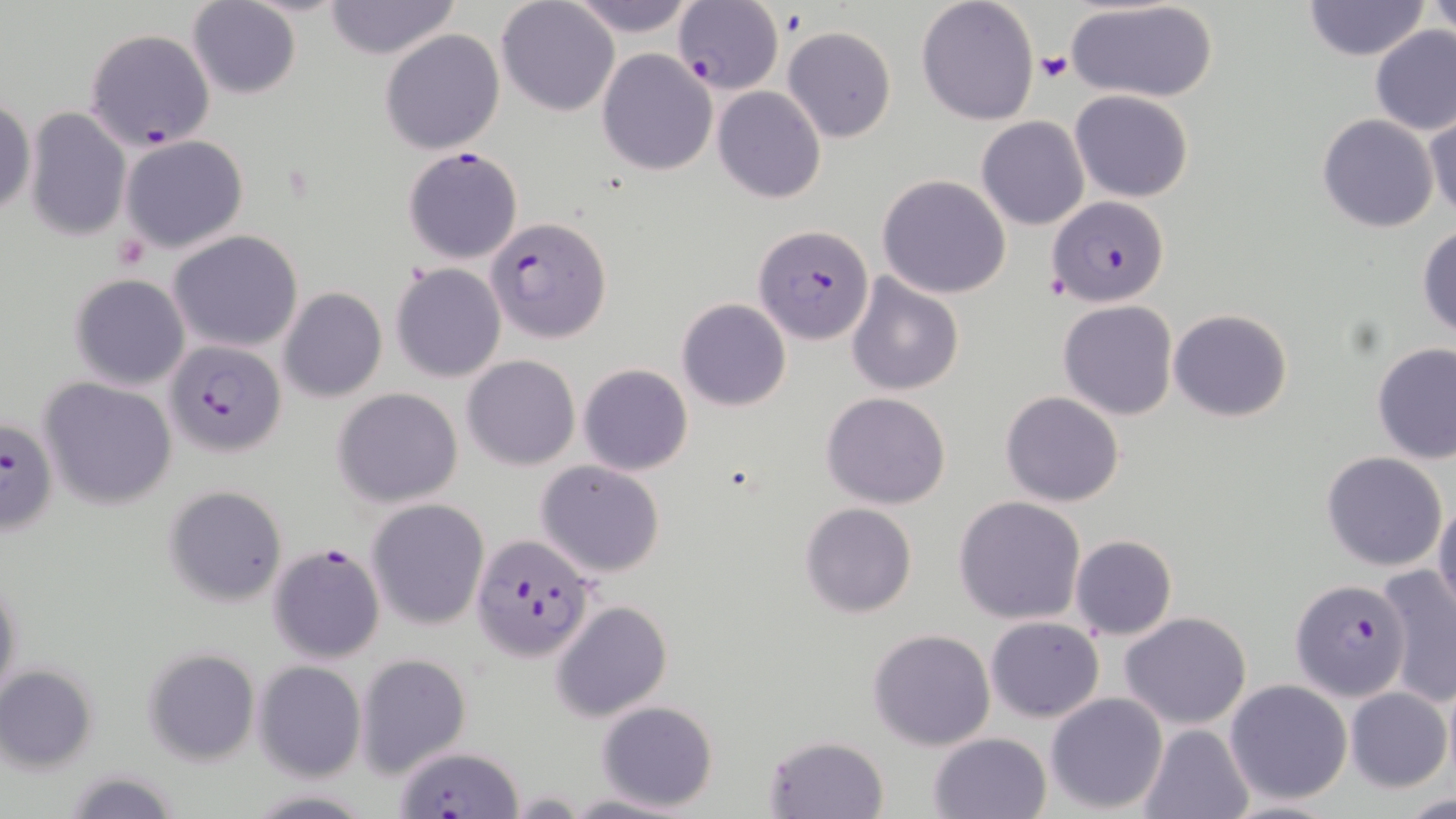 Approximate bounding boxes as (x1,y1)-(x2,y2) corner pairs in pixels. Plasmodium falciparum-infected red blood cell locations: (673,1)-(783,95), (85,28)-(214,150), (402,147)-(524,264), (1050,196)-(1169,305), (487,214)-(612,344), (754,224)-(874,347), (167,338)-(287,455), (0,415)-(59,533), (470,533)-(597,661), (267,543)-(385,666), (1290,579)-(1409,702), (395,747)-(520,818). Uninfected red blood cell locations: (496,0)-(619,116), (566,0)-(699,37), (916,0)-(1039,124), (1303,0)-(1430,61), (1425,0)-(1455,38), (187,1)-(302,100), (322,1)-(462,60), (1068,1)-(1219,104), (783,25)-(897,142), (1369,25)-(1456,136), (380,29)-(505,154), (596,47)-(718,176), (713,86)-(825,204), (1070,90)-(1195,203), (0,96)-(35,219), (25,107)-(130,242), (1423,109)-(1456,221), (1317,114)-(1439,234), (976,116)-(1089,230), (120,135)-(248,253), (877,175)-(1012,299), (1416,224)-(1456,340), (170,231)-(302,352), (391,263)-(505,382), (845,272)-(965,395), (69,274)-(190,391), (279,287)-(386,403), (677,298)-(790,411), (1059,300)-(1179,419), (1169,308)-(1293,423), (1372,341)-(1456,463), (462,355)-(580,470), (578,364)-(693,476), (37,376)-(177,510), (333,386)-(464,508), (822,391)-(951,510), (1001,391)-(1125,507), (1321,452)-(1448,572), (535,460)-(666,578), (165,485)-(287,606), (953,496)-(1086,625), (1433,497)-(1456,616), (367,498)-(489,629), (799,502)-(917,617), (1069,534)-(1177,640), (1378,567)-(1456,707), (0,572)-(23,715), (551,599)-(673,721), (1120,610)-(1252,728), (985,615)-(1104,722), (868,628)-(997,751), (142,647)-(261,765), (356,651)-(468,778), (254,661)-(366,782), (0,665)-(99,772), (1224,678)-(1353,805), (1345,687)-(1451,791), (1044,693)-(1168,812), (595,701)-(719,812), (1137,722)-(1254,818), (929,732)-(1054,819), (762,735)-(891,819), (64,768)-(181,819), (246,789)-(375,817), (508,791)-(585,816), (560,791)-(691,819), (1406,791)-(1456,817). Platelet locations: (781,10)-(807,37), (1037,51)-(1072,82), (113,232)-(151,270). Slide-level diagnosis: Plasmodium falciparum. Captured at 1000x magnification. One field of a larger specimen. Image is 1456×819 pixels. Light microscopy. May-Grünwald-Giemsa-stained preparation. Thin blood smear.